Identify the parasite.
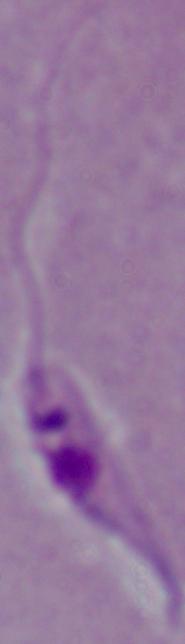
Leishmania.

1000x magnification. Micrograph.